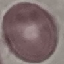

{
  "result": "negative for malaria parasites",
  "preparation": "thin smear",
  "image_type": "cell patch, automatically extracted from a larger field of view and resized to 64 × 64 pixels",
  "stain": "Giemsa",
  "capture": "smartphone camera at the microscope eyepiece"
}